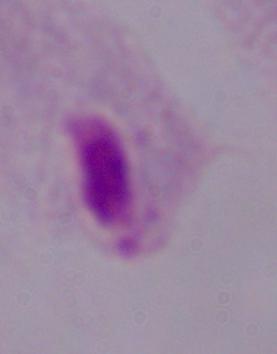
Summary:
  - Magnification: 1000x
  - Modality: photomicrograph
  - Identification: trichomonad